Report the malaria status of this cell.
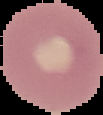
It is uninfected.

The area outside the segmented cell region is set to black. From a thin blood smear. Image is 103×115 pixels.